Report the malaria status of this cell.
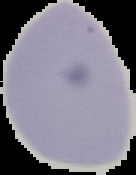

Uninfected.

From a thin blood smear. Image is 136×175 pixels. Cell region segmented out of the field of view; the surrounding area is masked to black.